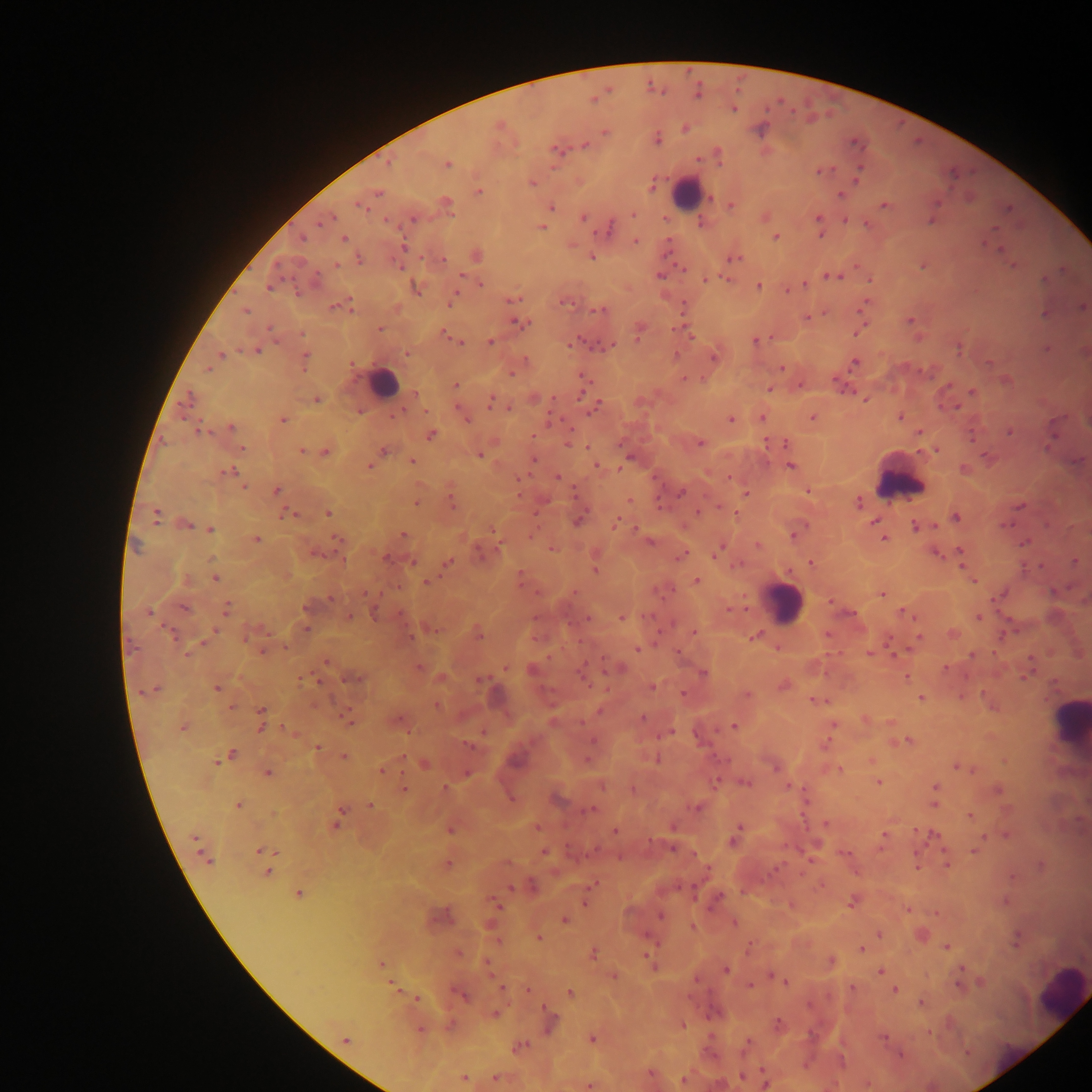

Approximate centers as {x, y} in pixels.
Summary:
  - Leukocyte locations: {685, 192}, {385, 383}, {904, 485}, {781, 612}, {1072, 723}, {1057, 988}
  - Malaria parasite locations: {782, 100}, {732, 108}, {792, 113}, {685, 129}, {658, 141}, {584, 144}, {554, 148}, {717, 151}, {562, 153}, {698, 160}, {387, 162}, {446, 165}, {834, 169}, {815, 171}, {822, 172}, {856, 181}, {532, 183}, {652, 187}, {376, 194}, {840, 195}, {712, 199}, {445, 202}, {358, 204}, {882, 204}, {551, 207}, {730, 207}, {1007, 209}, {633, 213}, {581, 216}, {816, 216}, {332, 218}, {412, 218}, {386, 220}, {844, 221}, {866, 223}, {316, 225}, {610, 227}, {543, 228}, {990, 228}, {821, 235}, {775, 237}, {345, 238}, {303, 239}, {635, 240}, {985, 241}, {403, 246}, {1001, 249}, {666, 252}, {593, 256}, {443, 257}, {737, 258}, {336, 265}, {855, 265}, {399, 266}, {922, 266}, {1013, 266}, {683, 269}, {460, 274}, {659, 275}, {825, 275}, {838, 277}, {725, 278}, {313, 279}, {705, 279}, {1043, 279}, {869, 280}, {482, 282}, {804, 284}, {268, 285}, {757, 285}, {786, 290}, {792, 290}, {456, 294}, {517, 298}, {511, 300}, {566, 302}, {449, 305}, {332, 308}, {351, 308}, {860, 309}, {595, 310}, {245, 311}, {600, 311}, {1043, 312}, {807, 318}, {908, 321}, {513, 323}, {522, 323}, {269, 328}, {379, 329}, {675, 329}, {671, 330}, {856, 333}, {446, 334}, {691, 337}, {637, 338}, {771, 338}, {919, 338}, {755, 340}, {489, 341}, {460, 342}, {569, 346}, {612, 347}, {958, 348}, {1045, 349}, {241, 350}, {256, 350}, {406, 352}, {676, 352}, {220, 355}, {305, 355}, {853, 362}, {988, 363}, {349, 364}, {782, 367}, {206, 368}, {303, 370}, {920, 370}, {511, 374}, {704, 378}, {685, 379}, {835, 380}, {455, 385}, {799, 385}, {770, 388}, {852, 391}, {972, 392}, {580, 394}, {861, 396}, {492, 397}, {187, 398}, {552, 399}, {864, 399}, {317, 400}, {489, 402}, {598, 403}, {508, 406}, {958, 407}, {404, 410}, {426, 412}, {592, 412}, {394, 417}, {899, 417}, {549, 418}, {760, 418}, {811, 418}, {282, 419}, {730, 419}, {468, 420}, {231, 427}, {570, 429}, {199, 432}, {211, 432}, {1009, 432}, {919, 433}, {430, 434}, {534, 434}, {972, 437}, {699, 443}, {767, 443}, {784, 444}, {1045, 446}, {586, 447}, {242, 448}, {935, 449}, {303, 450}, {384, 450}, {324, 452}, {481, 455}, {985, 456}, {413, 460}, {537, 460}, {534, 462}, {596, 465}, {789, 465}, {371, 467}, {619, 468}, {234, 470}, {222, 473}, {227, 473}, {522, 477}, {557, 477}, {516, 478}, {729, 478}, {243, 487}, {277, 489}, {808, 490}, {574, 491}, {680, 492}, {745, 494}, {519, 495}, {451, 499}, {416, 501}, {630, 501}, {858, 502}, {659, 503}, {1018, 505}, {453, 506}, {719, 506}, {699, 512}, {284, 513}, {297, 514}, {328, 514}, {735, 514}, {957, 517}, {617, 518}, {157, 519}, {1010, 522}, {874, 523}, {185, 524}, {614, 524}, {914, 526}, {935, 526}, {210, 528}, {635, 528}, {492, 529}, {334, 535}, {403, 535}, {794, 536}, {529, 537}, {883, 538}, {255, 539}, {339, 539}, {650, 542}, {1024, 542}, {722, 544}, {757, 545}, {497, 548}, {551, 549}, {959, 550}, {717, 551}, {479, 552}, {314, 554}, {683, 554}, {935, 554}, {715, 555}, {339, 557}, {386, 558}, {211, 559}, {342, 561}, {1076, 561}, {413, 563}, {449, 563}, {736, 563}, {810, 563}, {1042, 565}, {961, 567}, {1027, 567}, {594, 570}, {520, 573}, {523, 577}, {215, 578}, {697, 580}, {425, 582}, {974, 583}, {536, 592}, {574, 593}, {364, 595}, {881, 595}, {996, 597}, {331, 598}, {991, 598}, {227, 608}, {305, 608}, {728, 610}, {901, 611}, {373, 613}, {147, 614}, {400, 614}, {349, 617}, {587, 618}, {978, 618}, {621, 619}, {915, 621}, {305, 629}, {214, 631}, {1015, 631}, {692, 633}, {951, 634}, {480, 636}, {757, 636}, {412, 637}, {919, 637}, {1001, 637}, {246, 638}, {887, 638}, {284, 647}, {776, 648}, {637, 650}, {263, 651}, {678, 651}, {868, 651}, {188, 653}, {892, 654}, {994, 654}, {971, 655}, {547, 657}, {602, 658}, {1032, 658}, {326, 663}, {418, 666}, {506, 667}, {946, 668}, {703, 674}, {965, 676}, {300, 677}, {906, 677}, {1023, 677}, {358, 679}, {479, 680}, {320, 682}, {783, 686}, {650, 687}, {215, 689}, {139, 692}, {683, 693}, {984, 693}, {747, 694}, {960, 694}, {920, 698}, {811, 699}, {232, 706}, {261, 709}, {347, 709}, {643, 717}, {349, 719}, {865, 719}, {889, 721}, {581, 722}, {834, 725}, {733, 726}, {261, 727}, {282, 727}, {285, 728}, {406, 732}, {670, 732}, {592, 740}, {907, 740}, {825, 743}, {468, 745}, {317, 747}, {233, 754}, {345, 756}, {404, 758}, {658, 758}, {587, 760}, {871, 760}, {216, 761}, {424, 765}, {773, 766}, {955, 767}, {972, 769}, {841, 770}, {380, 771}, {267, 772}, {467, 774}, {878, 782}, {715, 783}, {748, 783}, {787, 786}, {934, 786}, {445, 787}, {405, 788}, {633, 788}, {997, 789}, {512, 798}, {806, 801}, {239, 804}, {933, 804}, {371, 805}, {698, 808}, {591, 809}, {341, 810}, {969, 816}, {826, 824}, {335, 825}, {740, 826}, {537, 827}, {915, 829}, {450, 830}, {615, 831}, {883, 834}, {936, 834}, {1005, 834}, {985, 836}, {193, 837}, {651, 842}, {732, 842}, {257, 850}, {672, 850}, {973, 851}, {543, 852}, {207, 859}, {210, 863}, {507, 863}, {1040, 864}, {447, 865}, {945, 865}, {918, 866}, {776, 868}, {706, 870}, {268, 871}, {772, 871}, {1013, 876}, {510, 888}, {298, 893}, {583, 902}, {1004, 902}, {851, 903}, {498, 906}, {908, 909}, {936, 911}, {660, 916}, {563, 920}, {733, 923}, {693, 926}, {878, 934}, {538, 937}, {1015, 939}, {748, 947}, {946, 948}, {861, 949}, {458, 952}, {593, 952}, {647, 956}, {832, 962}, {380, 963}, {961, 967}, {726, 970}, {880, 972}, {770, 975}, {614, 976}, {786, 982}, {980, 982}, {391, 983}, {748, 985}, {959, 986}, {502, 988}, {852, 988}, {895, 990}, {527, 991}, {569, 992}, {461, 996}, {416, 1000}, {920, 1003}, {542, 1007}, {495, 1014}, {779, 1024}, {684, 1025}, {420, 1029}, {929, 1032}, {882, 1037}, {591, 1039}, {345, 1041}, {964, 1050}, {903, 1054}, {760, 1068}, {649, 1074}, {740, 1076}, {464, 1077}, {495, 1077}, {683, 1080}, {767, 1084}, {589, 1086}
  - Image size: 1092×1092 pixels
  - Field of view: single
  - Preparation: thick blood smear
  - Country: Ghana
  - Capture: mobile-phone photograph through a microscope